State which parasite is depicted.
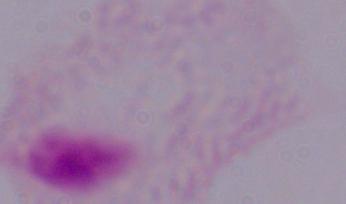
A trichomonad.

Captured at 1000x magnification. Micrograph.